Describe the morphology of the red blood cells.
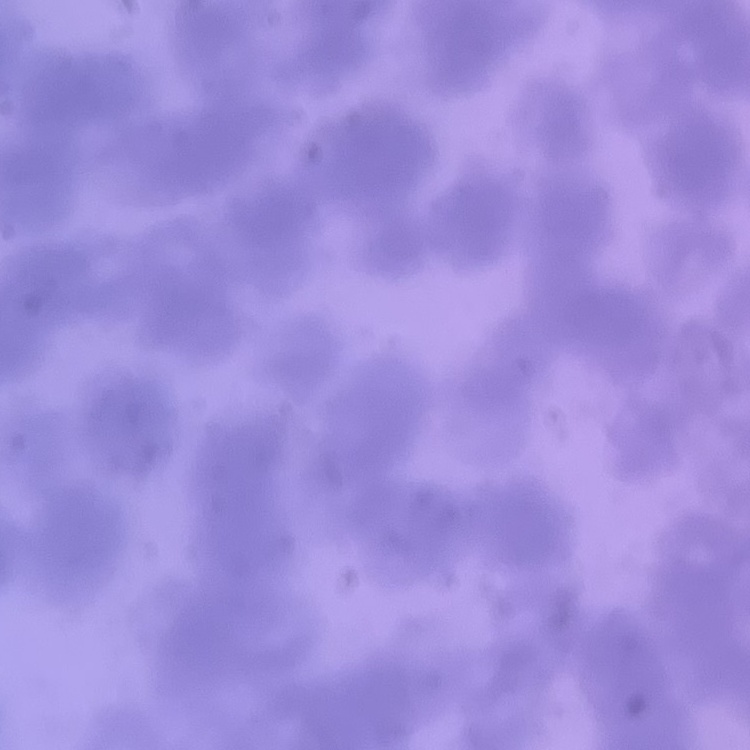
Rouleaux formation.

Summary:
  - Preparation: thin blood film
  - Image type: one tile cut from a larger photomicrograph
  - Stain: Field's or Giemsa